Comment on the morphology of the red blood cells.
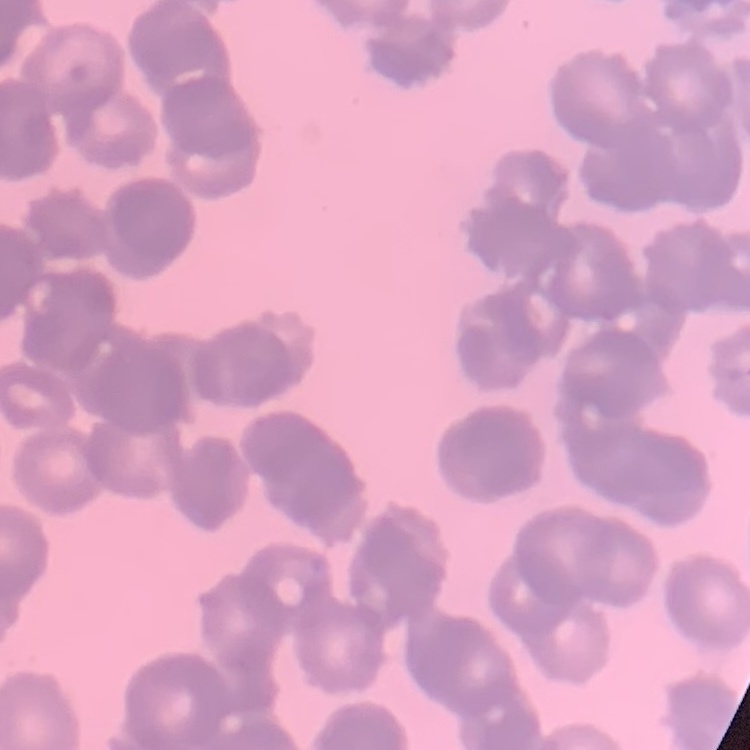
Rouleaux formation.

Thin peripheral smear. One tile cut from a larger photomicrograph. Field's or Giemsa stain.